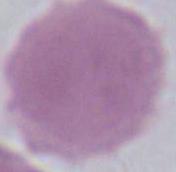

Summary:
  - Magnification: 1000x
  - Modality: micrograph
  - Identification: red blood cell